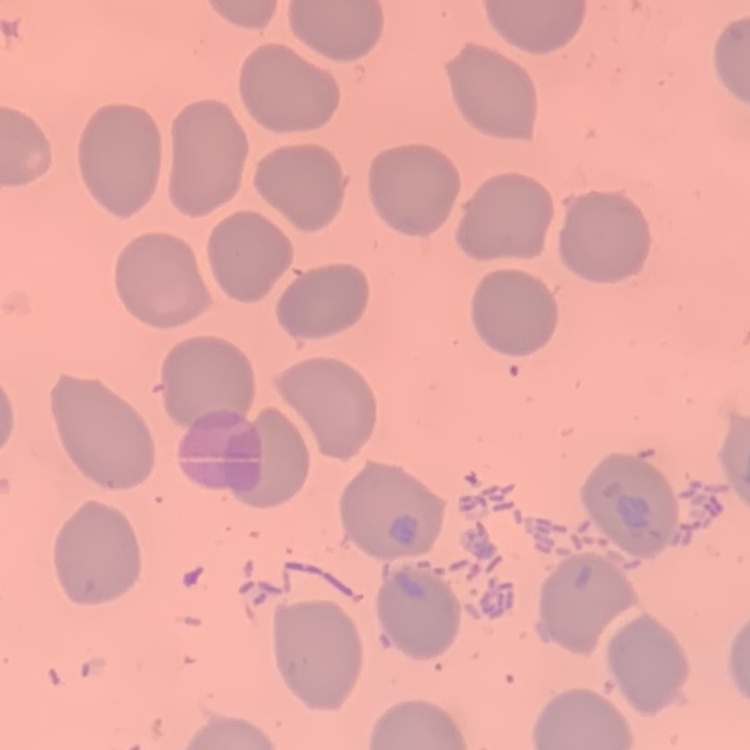

Summary:
  - Erythrocyte morphology: no rouleaux formation
  - Image type: one tile cut from a larger photomicrograph
  - Stain: Field's or Giemsa
  - Preparation: thin peripheral smear